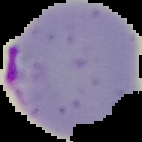
Summary:
  - Malaria status: parasitized
  - Image size: 142×142 pixels
  - Image type: cell region segmented out of the field of view; surrounding area masked to black
  - Preparation: thin blood film